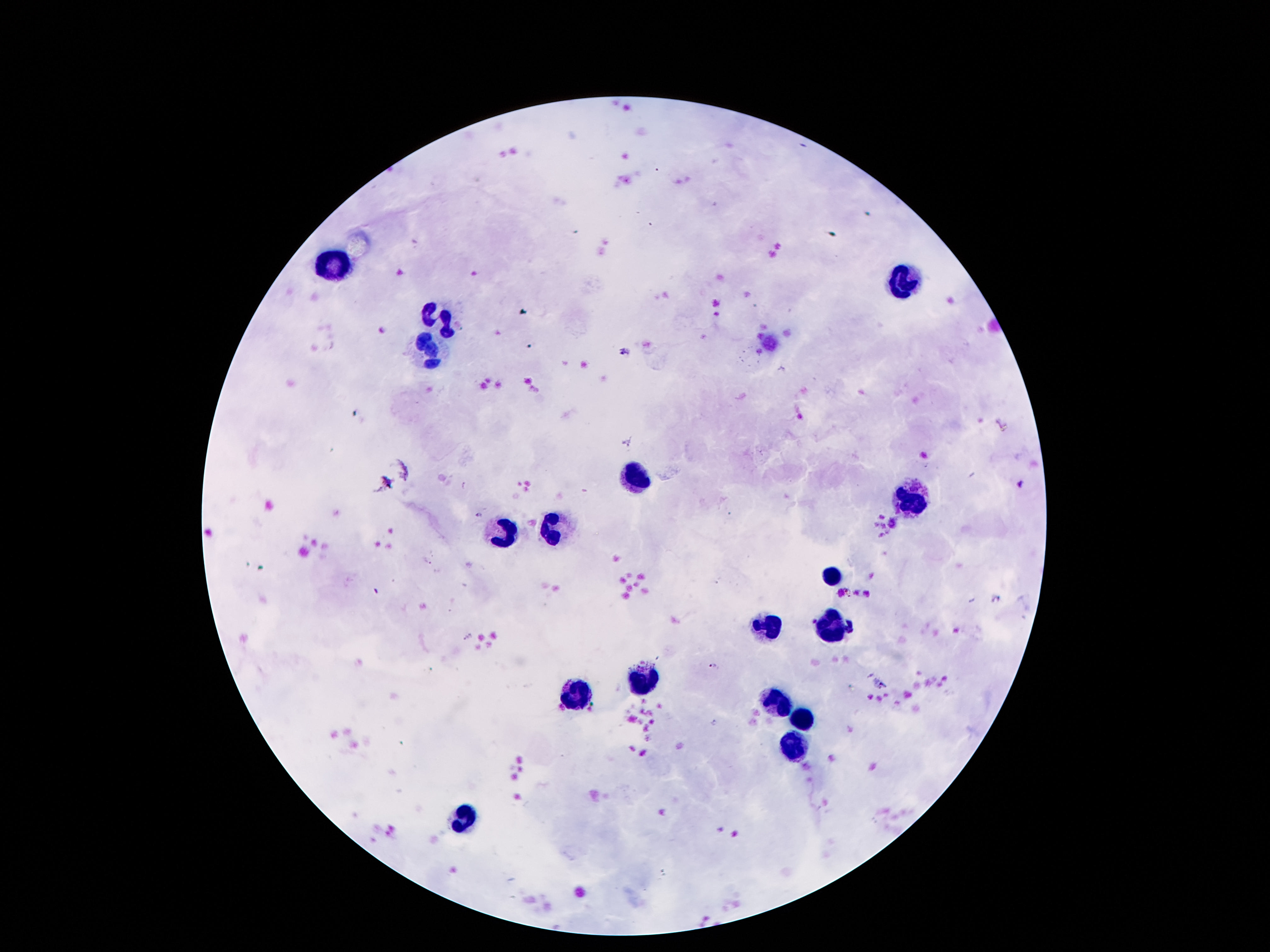 Approximate centers as [x, y] in pixels. Leukocyte locations: [335, 262], [901, 279], [442, 316], [430, 348], [636, 475], [912, 498], [550, 529], [503, 531], [835, 574], [764, 624], [835, 624], [643, 676], [574, 691], [779, 699], [804, 719], [796, 747], [462, 818]. Giemsa stain. Image is 1270×952 pixels. Photographed through the microscope eyepiece with a smartphone camera. Patient malaria status: uninfected. Thick blood smear. 100x magnification. Single field of view.